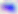

Summary:
  - Modality: micrograph
  - Magnification: 400x
  - Identification: Toxoplasma gondii